Identify the preparation type.
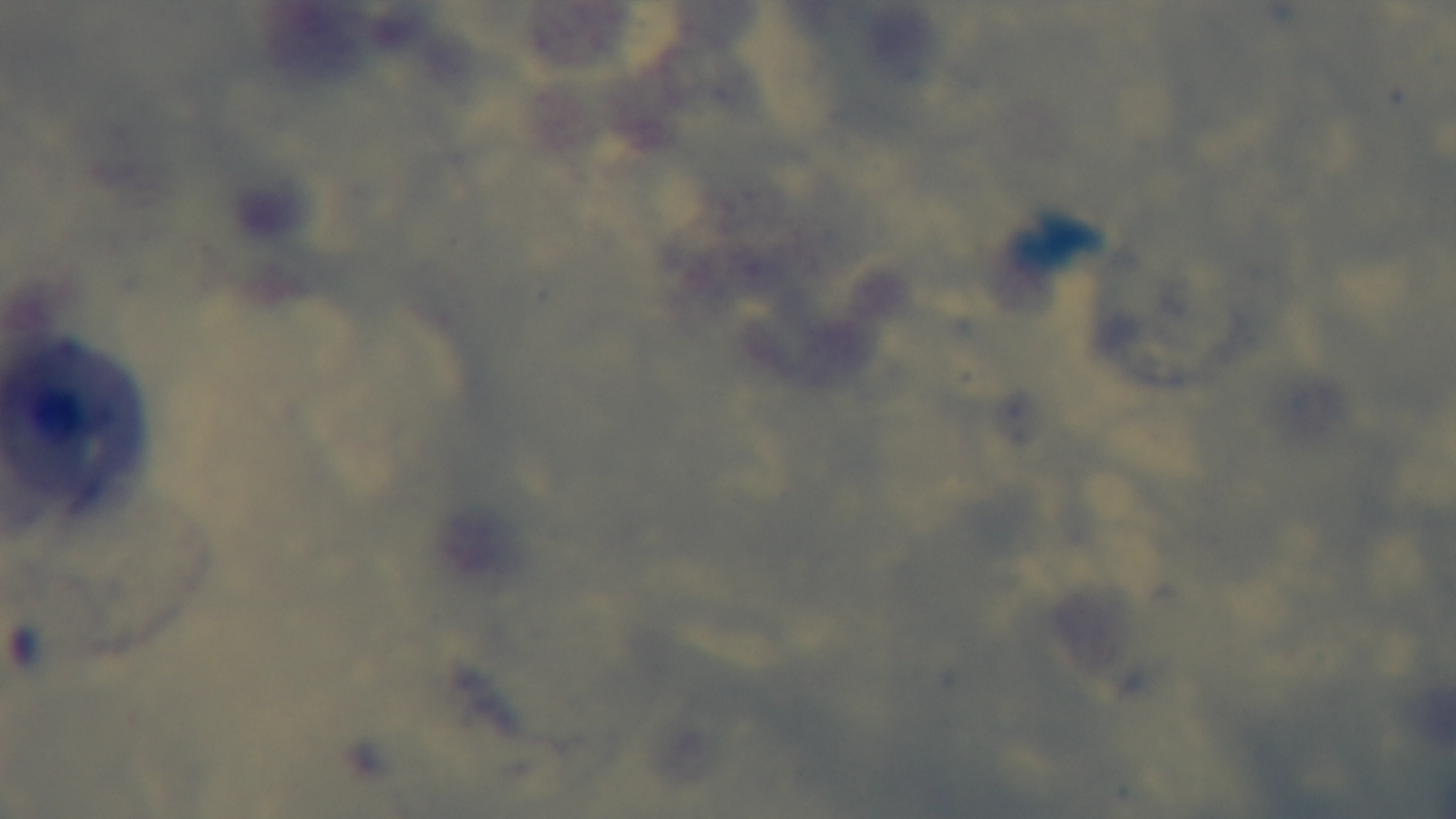
A thick smear.

Summary:
  - Malaria status: negative
  - Capture: mounted 4K digital camera
  - Field of view: single
  - Objective: 100x oil immersion
  - Modality: light microscopy
  - Stain: Giemsa